Locate every blood parasite and identify its species.
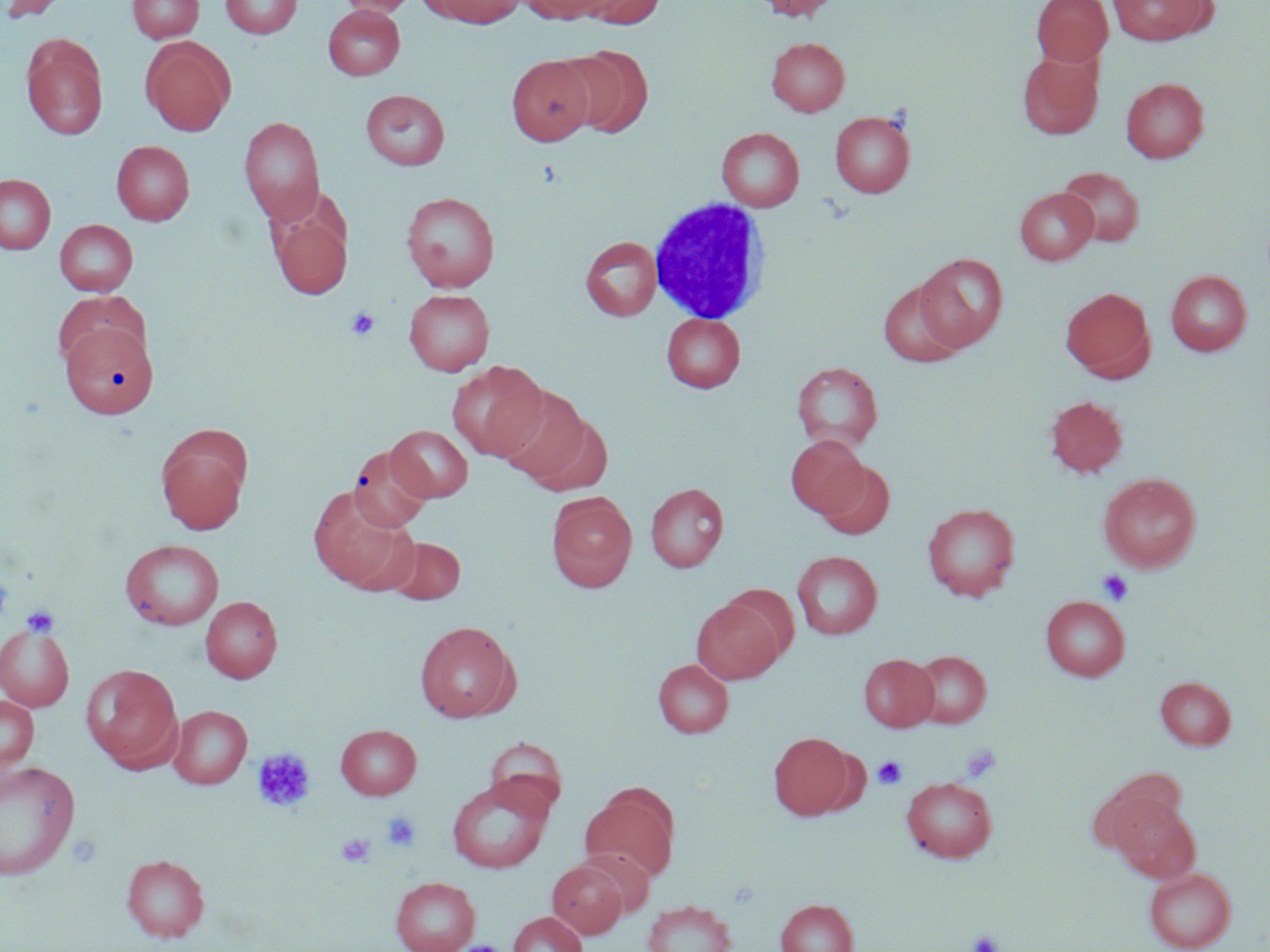
No blood parasites seen.

Approximate bounding boxes as [x1, y1, x2, y2] in pixels. Platelet locations: [345, 307, 380, 341], [0, 570, 13, 626], [1097, 570, 1133, 606], [20, 604, 60, 637], [961, 743, 1002, 782], [252, 747, 316, 812], [872, 756, 907, 789], [381, 811, 422, 852], [336, 834, 376, 868], [966, 929, 1004, 952], [461, 940, 502, 952]. White blood cell locations: [648, 197, 771, 325]. Uninfected red blood cell locations: [0, 0, 74, 22], [127, 0, 203, 43], [220, 0, 302, 39], [337, 0, 417, 16], [431, 0, 525, 28], [519, 0, 612, 24], [579, 0, 665, 28], [752, 0, 840, 21], [1031, 0, 1113, 67], [1107, 0, 1214, 45], [323, 5, 405, 80], [21, 34, 109, 140], [141, 37, 236, 136], [767, 37, 849, 116], [558, 47, 653, 137], [1017, 51, 1103, 139], [506, 55, 596, 146], [1121, 77, 1209, 163], [361, 89, 450, 170], [830, 111, 915, 198], [238, 116, 325, 224], [717, 127, 804, 211], [111, 140, 194, 225], [1058, 167, 1145, 247], [0, 174, 55, 254], [1015, 188, 1098, 265], [401, 192, 500, 292], [271, 205, 352, 300], [55, 219, 138, 296], [580, 236, 662, 321], [915, 253, 1007, 351], [1166, 270, 1252, 356], [878, 279, 965, 367], [1060, 287, 1154, 379], [404, 289, 494, 375], [52, 290, 147, 372], [661, 313, 745, 392], [60, 320, 158, 419], [447, 360, 549, 462], [792, 361, 883, 451], [494, 385, 596, 486], [1044, 395, 1129, 478], [156, 425, 252, 533], [387, 425, 473, 501], [786, 435, 869, 518], [348, 445, 433, 532], [816, 460, 895, 539], [1099, 472, 1201, 573], [645, 482, 729, 572], [308, 488, 415, 591], [546, 492, 637, 592], [922, 502, 1020, 601], [386, 536, 465, 604], [120, 539, 224, 630], [792, 550, 883, 640], [201, 596, 282, 683], [1040, 596, 1130, 681], [691, 598, 784, 683], [415, 620, 519, 722], [0, 624, 75, 712], [910, 650, 991, 728], [858, 654, 939, 732], [653, 659, 733, 737], [81, 663, 183, 771], [1155, 676, 1236, 751], [0, 695, 38, 773], [168, 705, 252, 788], [336, 724, 421, 799], [768, 732, 854, 821], [485, 737, 568, 818], [0, 760, 80, 881], [1091, 771, 1188, 855], [446, 776, 553, 873], [901, 776, 997, 862], [580, 783, 680, 884], [1110, 794, 1200, 883], [577, 848, 655, 917], [121, 854, 209, 941], [547, 859, 628, 938], [1144, 867, 1236, 952], [390, 875, 480, 952], [776, 898, 859, 952], [643, 900, 737, 952], [508, 911, 587, 952], [457, 941, 506, 952]. Slide-level diagnosis: no evidence of blood parasites. Thin blood film. Image is 1270×952 pixels. Light microscopy. May-Grünwald-Giemsa-stained preparation. One field of a larger specimen. Captured at 1000x magnification.